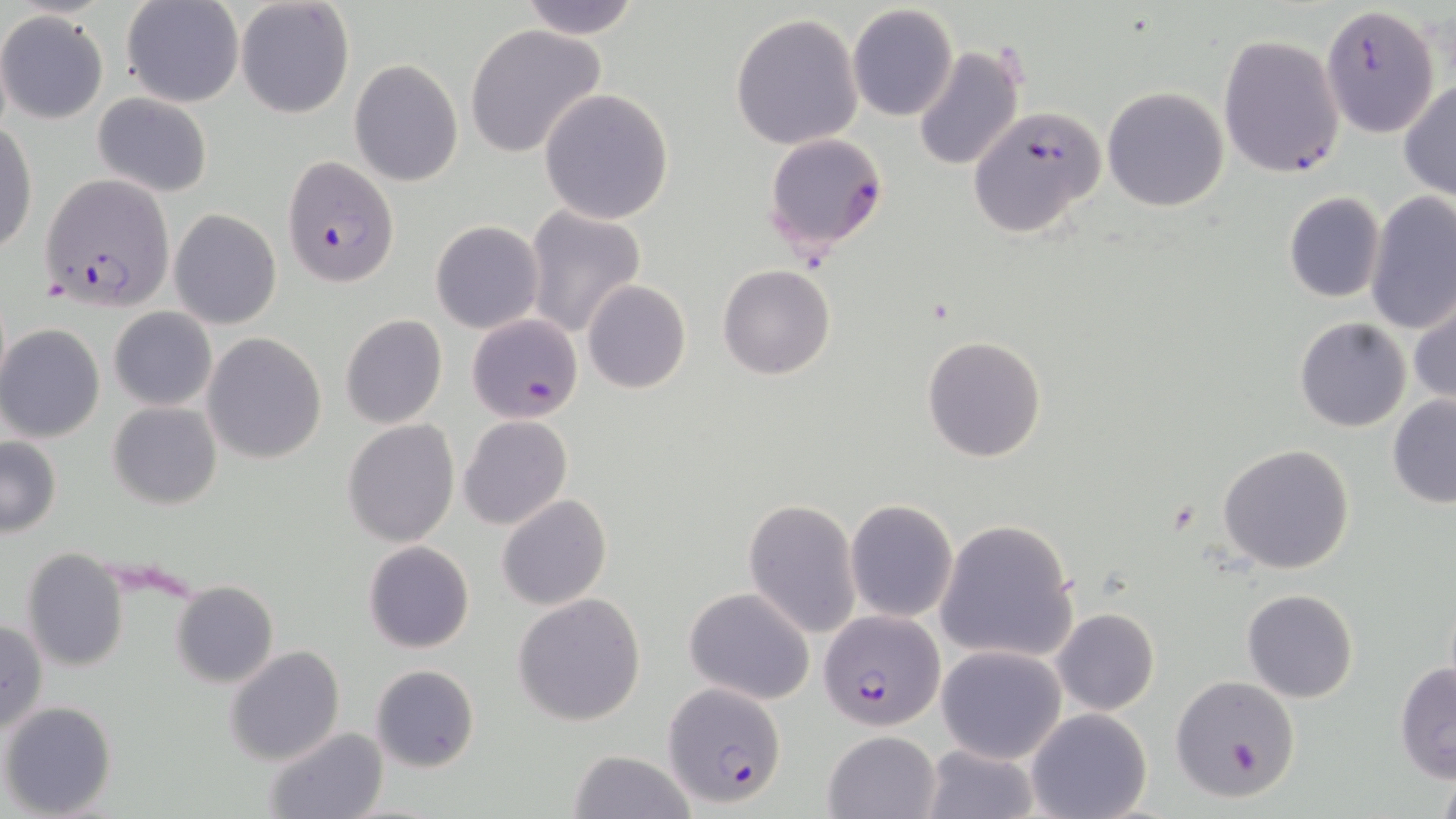
Approximate bounding boxes as named x1/y1/x2/y2 corners in pixels. Uninfected red blood cell locations: (x1=121, y1=0, x2=243, y2=108), (x1=235, y1=0, x2=355, y2=119), (x1=518, y1=0, x2=642, y2=40), (x1=847, y1=4, x2=959, y2=123), (x1=0, y1=11, x2=108, y2=125), (x1=730, y1=12, x2=863, y2=151), (x1=465, y1=23, x2=606, y2=158), (x1=913, y1=43, x2=1027, y2=172), (x1=349, y1=59, x2=463, y2=187), (x1=1399, y1=80, x2=1456, y2=202), (x1=1101, y1=87, x2=1230, y2=212), (x1=539, y1=88, x2=674, y2=224), (x1=93, y1=93, x2=213, y2=197), (x1=0, y1=122, x2=37, y2=258), (x1=1364, y1=191, x2=1456, y2=338), (x1=1283, y1=192, x2=1384, y2=304), (x1=524, y1=205, x2=647, y2=341), (x1=170, y1=208, x2=281, y2=329), (x1=430, y1=220, x2=544, y2=334), (x1=718, y1=265, x2=836, y2=380), (x1=582, y1=280, x2=690, y2=392), (x1=1409, y1=287, x2=1456, y2=411), (x1=108, y1=307, x2=217, y2=410), (x1=340, y1=314, x2=448, y2=429), (x1=1294, y1=316, x2=1411, y2=431), (x1=0, y1=324, x2=105, y2=442), (x1=202, y1=332, x2=327, y2=464), (x1=922, y1=335, x2=1048, y2=463), (x1=1386, y1=393, x2=1456, y2=509), (x1=108, y1=401, x2=223, y2=510), (x1=458, y1=415, x2=571, y2=531), (x1=343, y1=420, x2=460, y2=546), (x1=0, y1=437, x2=62, y2=536), (x1=1217, y1=444, x2=1355, y2=575), (x1=496, y1=494, x2=613, y2=610), (x1=743, y1=497, x2=861, y2=638), (x1=845, y1=500, x2=957, y2=622), (x1=935, y1=519, x2=1079, y2=665), (x1=362, y1=540, x2=476, y2=654), (x1=20, y1=548, x2=130, y2=672), (x1=171, y1=580, x2=278, y2=689), (x1=1242, y1=588, x2=1358, y2=703), (x1=512, y1=593, x2=646, y2=726), (x1=1051, y1=608, x2=1160, y2=715), (x1=1, y1=617, x2=48, y2=737), (x1=225, y1=645, x2=345, y2=766), (x1=937, y1=645, x2=1066, y2=762), (x1=1393, y1=662, x2=1456, y2=783), (x1=370, y1=663, x2=479, y2=773), (x1=1169, y1=674, x2=1302, y2=804), (x1=2, y1=700, x2=117, y2=818), (x1=1025, y1=708, x2=1152, y2=819), (x1=261, y1=727, x2=386, y2=819), (x1=821, y1=729, x2=941, y2=819), (x1=918, y1=743, x2=1039, y2=819), (x1=568, y1=750, x2=695, y2=819). Plasmodium falciparum-infected red blood cell locations: (x1=1320, y1=2, x2=1440, y2=140), (x1=1218, y1=34, x2=1346, y2=179), (x1=967, y1=106, x2=1106, y2=237), (x1=763, y1=133, x2=890, y2=255), (x1=280, y1=155, x2=400, y2=287), (x1=38, y1=172, x2=175, y2=310), (x1=466, y1=314, x2=584, y2=423), (x1=820, y1=610, x2=943, y2=730), (x1=661, y1=685, x2=786, y2=802). Slide-level diagnosis: Plasmodium falciparum. May-Grünwald-Giemsa stain. Light microscopy. Image is 1456×819 pixels. Thin blood smear. Single field of view. 1000x magnification.